Locate every Plasmodium parasite.
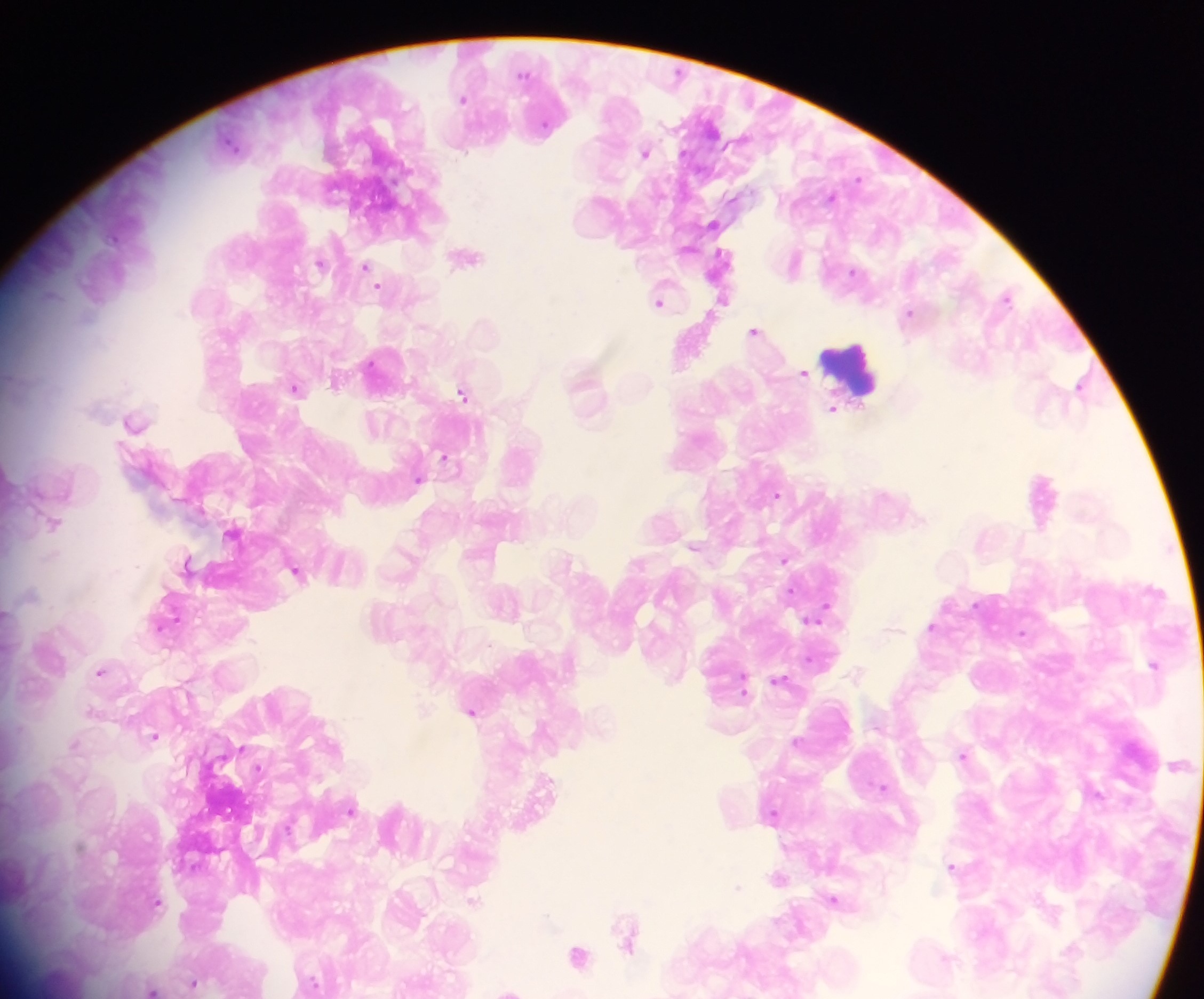

Approximate centers as x y in pixels.
Plasmodium parasites: 524 73; 462 98; 232 144; 645 152; 858 177; 832 196; 711 223; 468 255; 794 261; 320 262; 365 265; 853 270; 380 287; 1007 295; 723 300; 659 302; 909 312; 755 330; 804 372; 335 381; 1079 384; 295 387; 463 393; 832 407; 135 420; 446 457; 417 478; 777 494; 53 522; 232 533; 694 546; 785 559; 188 561; 296 570; 791 590; 6 612; 819 613; 166 622; 931 626; 1022 632; 1154 664; 101 670; 779 679; 744 686; 91 710; 472 711; 154 736; 796 739; 75 743; 963 755; 883 785; 352 808; 773 813; 952 866; 777 877; 737 886; 834 898; 474 899; 157 901; 626 933; 1072 947; 577 954; 193 983; 312 983; 153 988; 509 988.

Leukocyte locations: 855 369. One field of view. Image is 1204×999 pixels. Photographed through a microscope with a mobile-phone camera. Collected in Ghana. Thick blood smear.